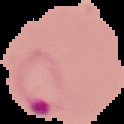 From a thin blood film. Malaria status: parasitized. Image is 124×124 pixels. Cell region segmented out of the field of view; the surrounding area is masked to black.